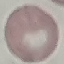
Summary:
  - Malaria status: uninfected
  - Capture: smartphone camera at the microscope eyepiece
  - Image type: automatically extracted cell patch, resized to 64 × 64 pixels
  - Preparation: thin blood film
  - Stain: Giemsa